Locate and identify every blood parasite.
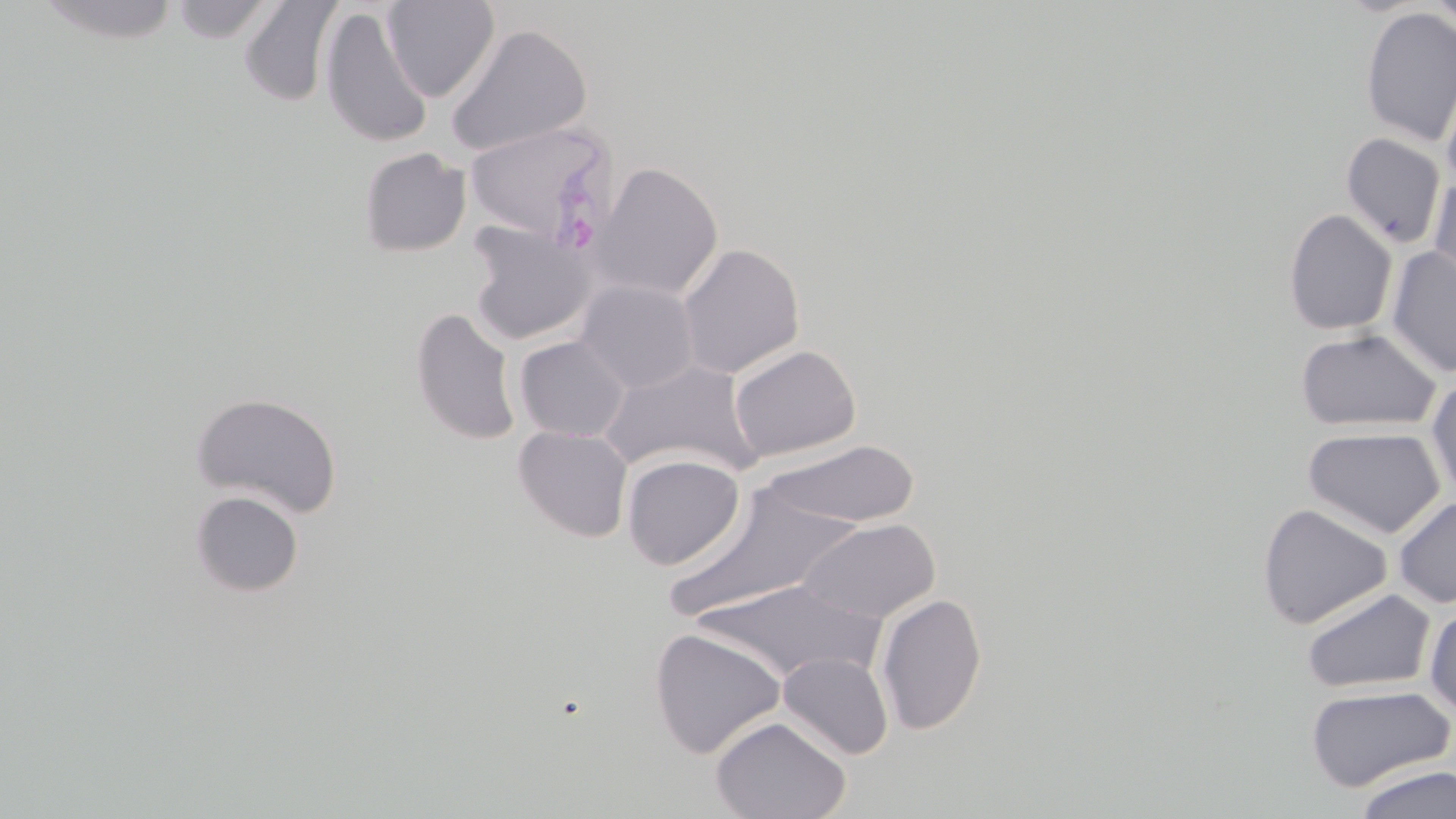
Approximate bounding boxes as (x1, y1, x2, y2) in pixels.
Plasmodium ovale-infected red blood cells: (462, 121, 619, 245).
No Plasmodium falciparum, Plasmodium malariae, Plasmodium vivax, Babesia divergens, or Trypanosoma brucei observed.

slide-level diagnosis = Plasmodium ovale
field of view = single
magnification = 1000x
uninfected red blood cell locations = approximate bounding boxes as (x1, y1, x2, y2) in pixels: (34, 0, 183, 45), (172, 0, 277, 43), (238, 0, 342, 107), (382, 0, 500, 101), (1428, 0, 1456, 34), (319, 7, 433, 147), (1359, 7, 1456, 148), (445, 23, 592, 157), (1440, 69, 1456, 190), (1340, 133, 1446, 249), (358, 147, 471, 257), (590, 162, 723, 301), (1427, 176, 1456, 292), (1282, 208, 1398, 336), (465, 221, 596, 346), (677, 243, 805, 379), (1385, 247, 1456, 378), (574, 279, 700, 393), (410, 307, 522, 446), (1295, 327, 1442, 433), (515, 336, 630, 441), (728, 344, 862, 462), (599, 359, 764, 478), (1427, 376, 1456, 501), (189, 391, 343, 519), (513, 425, 633, 542), (1303, 426, 1446, 538), (758, 439, 923, 528), (512, 442, 744, 554), (621, 454, 745, 570), (668, 481, 858, 621), (189, 489, 305, 597), (1393, 494, 1456, 608), (1257, 503, 1392, 630), (796, 517, 941, 623), (693, 578, 883, 683), (1301, 588, 1436, 694), (875, 592, 987, 736), (1424, 605, 1456, 718), (649, 627, 787, 759), (778, 652, 894, 759), (1303, 684, 1456, 792), (710, 715, 851, 819), (1354, 764, 1456, 819)
image size = 1456×819 pixels
preparation = thin blood film
modality = optical microscopy
stain = May-Grünwald-Giemsa